Classify this cell by malaria status.
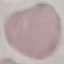

Uninfected.

Summary:
  - Image type: automatically extracted cell patch, resized to 64 × 64 pixels
  - Capture: smartphone through the microscope eyepiece
  - Preparation: thin smear
  - Stain: Giemsa